Locate every malaria parasite.
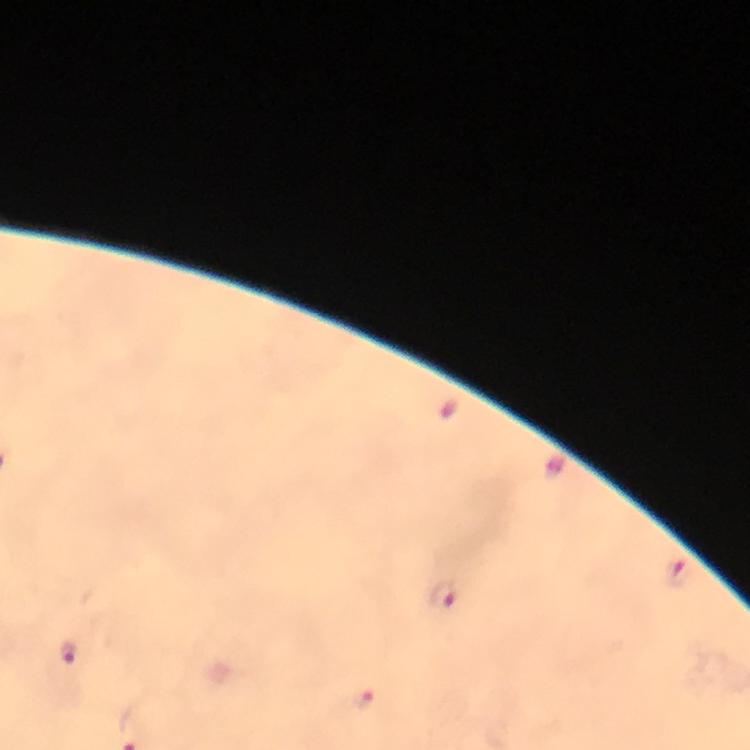
Approximate centers as (x, y) in pixels.
Malaria parasites: (679, 574), (441, 595), (70, 652), (362, 699).

preparation = thick blood smear
image size = 750×750 pixels
context = from a diagnostic examination for malaria
capture = smartphone mounted on the microscope
stain = Giemsa
immersion oil = applied
magnification = 100x
cropped from = one field of view